Identify the parasite.
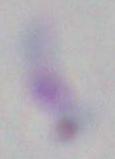
This is Toxoplasma gondii.

Summary:
  - Modality: micrograph
  - Magnification: 1000x